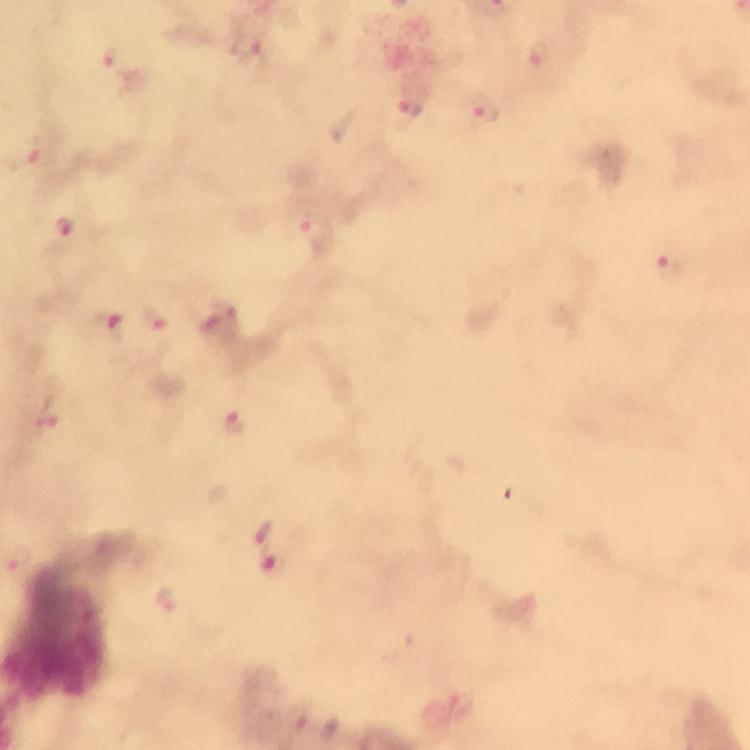 Approximate centers as {x, y} in pixels. Plasmodium parasite locations: {247, 47}, {540, 56}, {111, 57}, {410, 106}, {483, 113}, {32, 152}, {66, 225}, {314, 233}, {673, 268}, {153, 319}, {109, 327}, {47, 416}, {232, 423}, {263, 535}, {18, 557}, {167, 602}, {296, 719}. 100x magnification. From a diagnostic examination for malaria. Immersion oil was used. Thick blood film. Giemsa-stained preparation. Image is 750×750 pixels. Cropped region of a single field of view. Photographed with a smartphone mounted on the microscope.